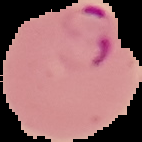
result = Plasmodium parasites identified
preparation = thin blood film
image type = cell region segmented out of the field of view; surrounding area masked to black
image size = 142×142 pixels